Give the position of every leukocyte visible.
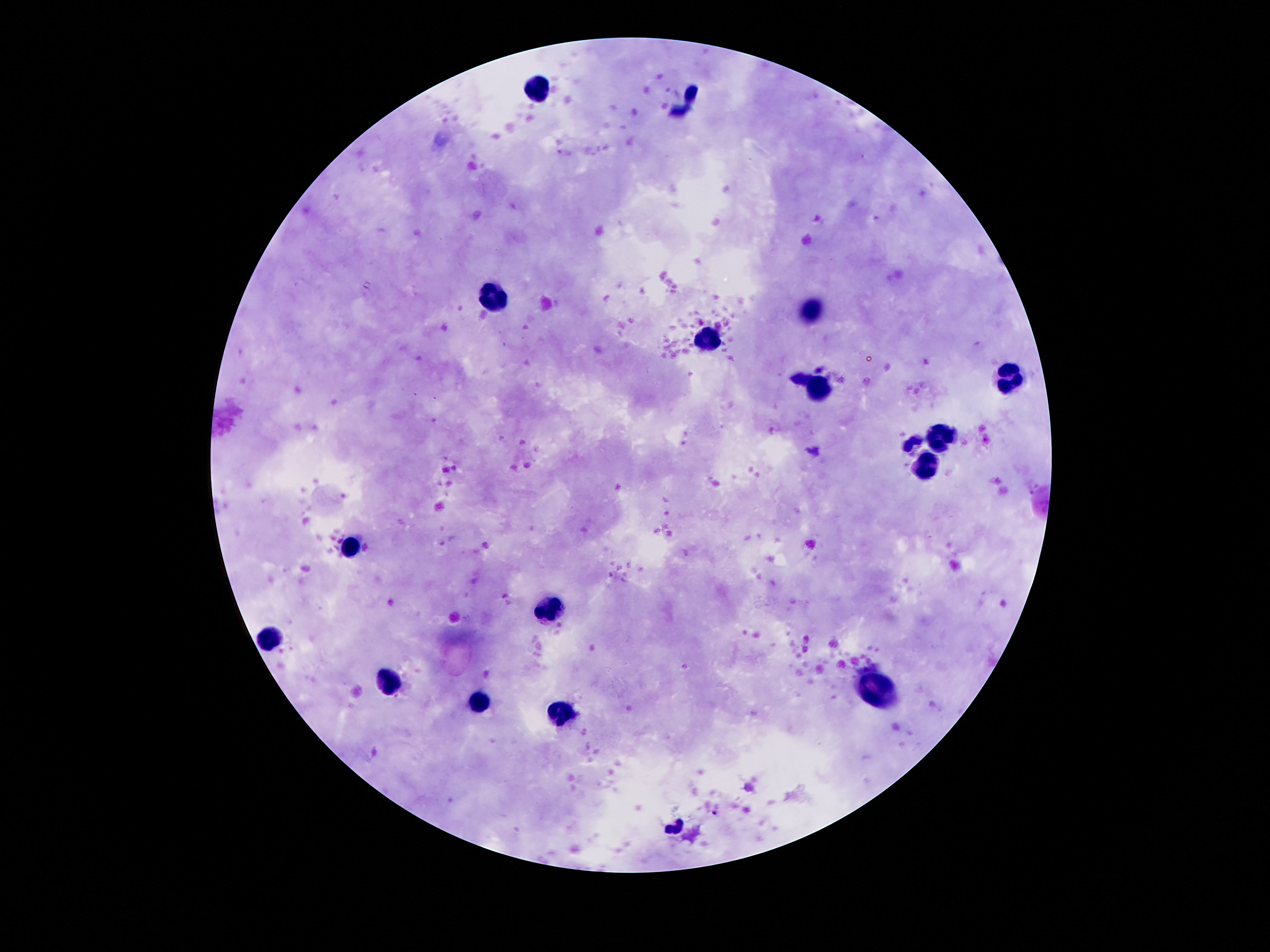
Approximate object centers, in pixels from the top-left corner.
Leukocytes: (x=538, y=89), (x=496, y=291), (x=813, y=307), (x=708, y=342), (x=1013, y=377), (x=824, y=394), (x=941, y=436), (x=927, y=470), (x=353, y=547), (x=548, y=610), (x=273, y=635), (x=387, y=684), (x=876, y=690), (x=477, y=701), (x=561, y=711).

field of view = single
image size = 1270×952 pixels
magnification = 100x
preparation = thick blood smear
stain = Giemsa
patient malaria status = not infected
capture = smartphone camera through the microscope eyepiece